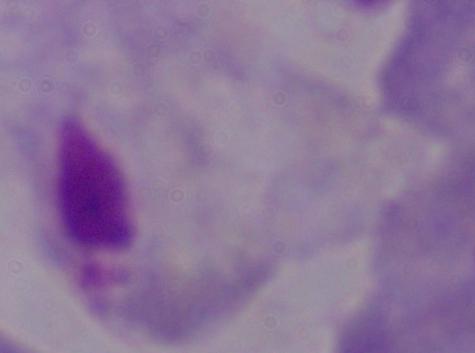
Micrograph. Captured at 1000x magnification. A trichomonad is seen.